Locate every leukocyte (white blood cell).
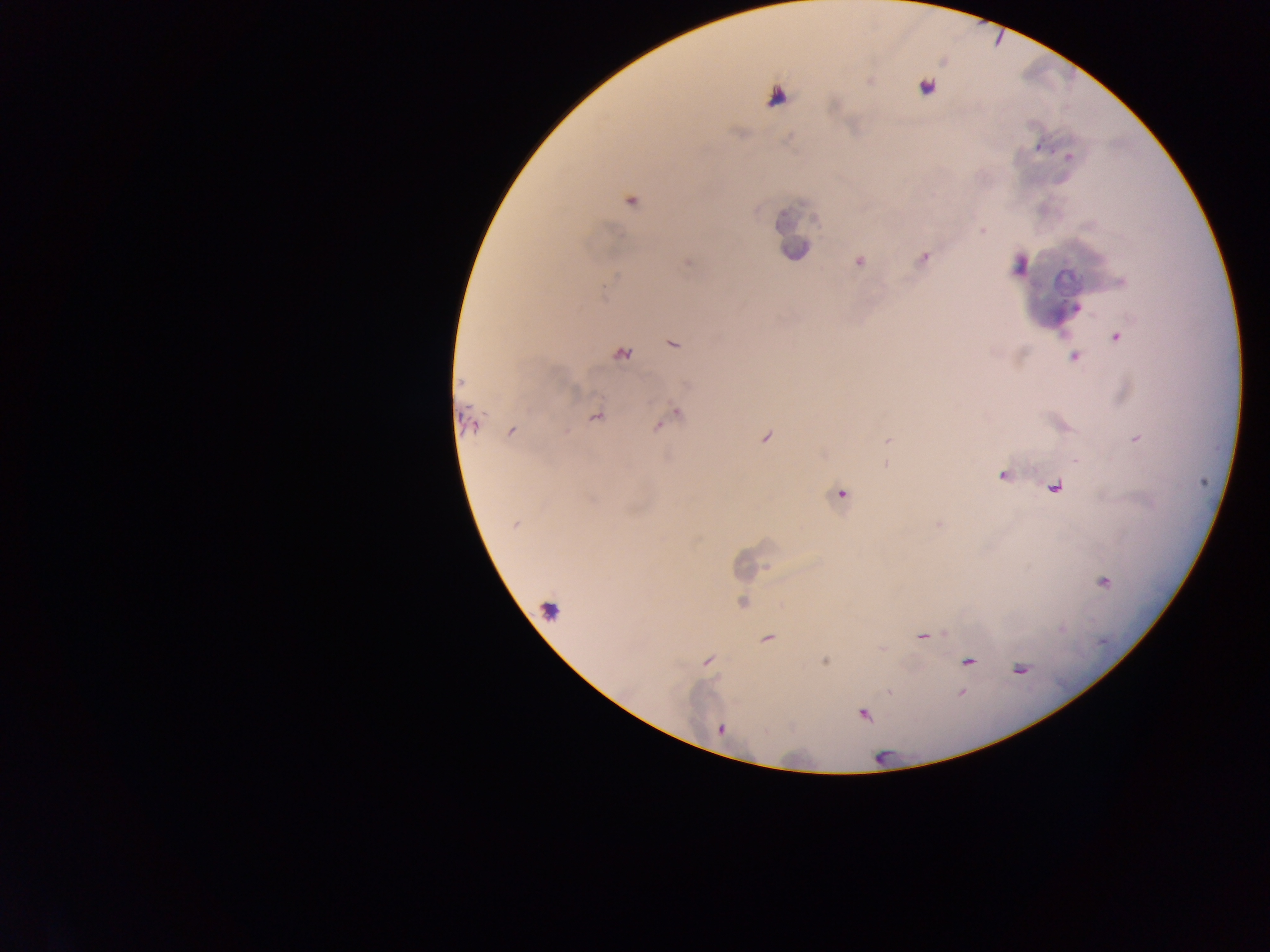
Approximate centers as [x, y] in pixels.
Leukocytes: [775, 98], [796, 250], [1018, 265].

Summary:
  - Plasmodium parasite locations: [869, 82], [926, 86], [1068, 157], [630, 201], [982, 231], [922, 258], [858, 261], [687, 262], [1120, 282], [1076, 307], [1116, 336], [672, 342], [620, 354], [1074, 356], [461, 382], [674, 413], [595, 415], [663, 421], [470, 422], [657, 425], [511, 431], [765, 438], [1136, 438], [888, 439], [885, 465], [1002, 475], [1054, 486], [840, 494], [515, 524], [939, 524], [1103, 582], [742, 603], [921, 636], [767, 638], [707, 660], [824, 660], [967, 661], [1019, 669], [889, 692], [960, 692], [862, 714], [721, 729]
  - Preparation: thick blood film
  - Field of view: single
  - Image size: 1270×952 pixels
  - Capture: mobile-phone photograph through a microscope
  - Country: Ghana